Report the malaria status of this cell.
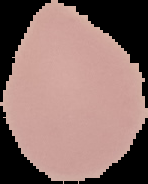

Uninfected.

Summary:
  - Image size: 148×184 pixels
  - Preparation: thin blood film
  - Image type: cell region segmented out of the field of view; surrounding area masked to black